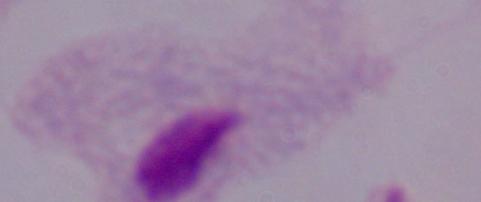

Summary:
  - Modality: photomicrograph
  - Magnification: 1000x
  - Identification: trichomonad